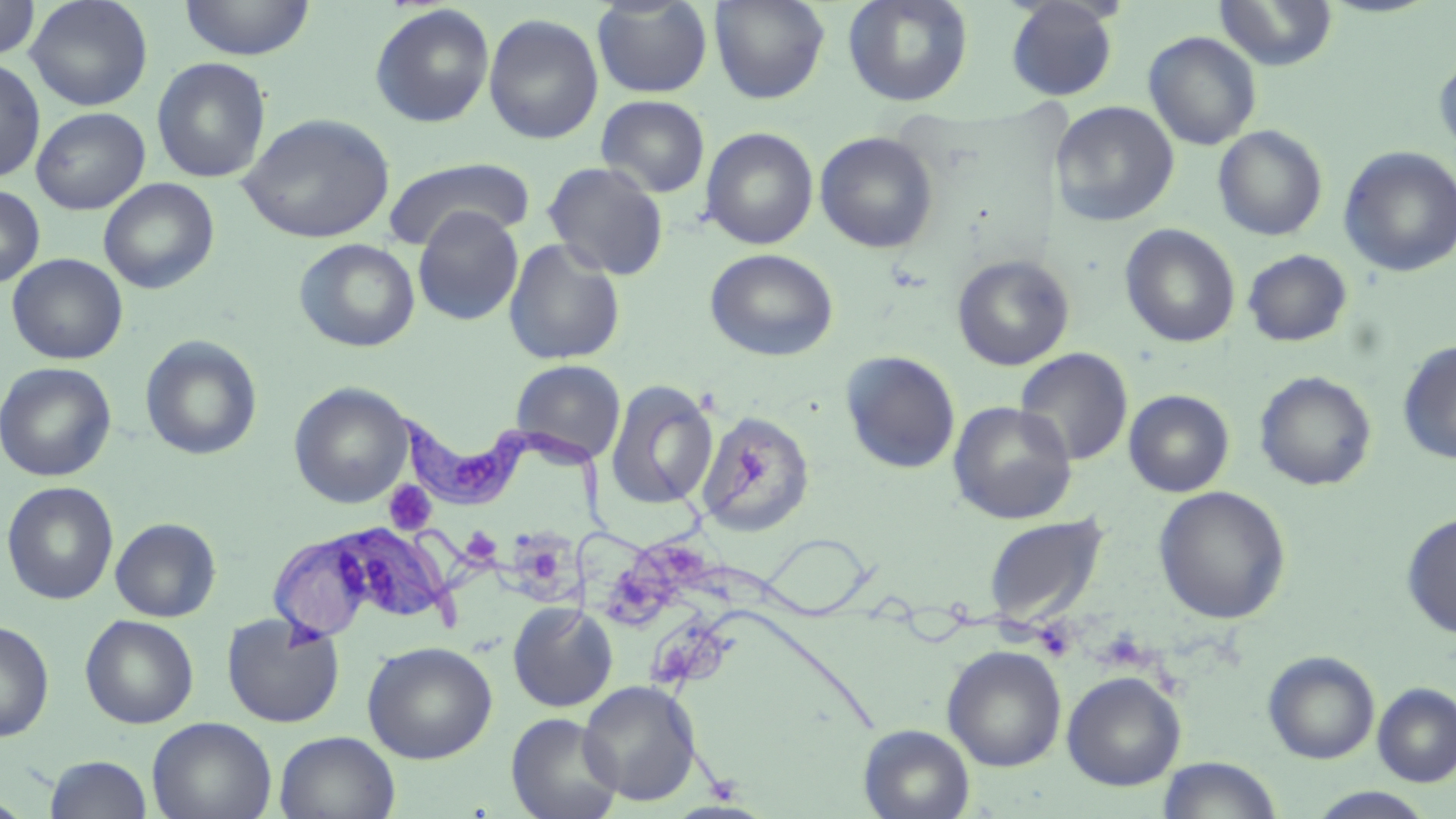
Summary:
  - Coordinate format: approximate bounding boxes as (x1,y1)-(x2,y2) corner pairs in pixels
  - Platelet locations: (383,481)-(436,535), (1032,618)-(1077,661), (1095,628)-(1152,671)
  - Uninfected red blood cell locations: (0,0)-(40,61), (25,0)-(153,111), (178,0)-(315,60), (591,0)-(713,98), (709,0)-(830,104), (842,0)-(973,107), (1005,0)-(1120,101), (1214,0)-(1338,71), (369,3)-(495,129), (483,13)-(604,145), (1143,31)-(1262,151), (1433,55)-(1456,159), (152,57)-(271,183), (0,58)-(45,183), (596,94)-(710,197), (1050,101)-(1179,228), (31,107)-(149,214), (238,112)-(395,244), (1212,125)-(1328,241), (700,127)-(819,249), (815,132)-(938,254), (1338,146)-(1456,278), (382,157)-(534,251), (542,161)-(670,281), (99,177)-(219,294), (0,185)-(45,289), (412,206)-(524,326), (1120,224)-(1240,348), (294,238)-(421,353), (502,238)-(626,366), (705,248)-(838,361), (1242,249)-(1351,347), (6,253)-(128,364), (952,255)-(1074,370), (139,335)-(263,460), (1397,340)-(1456,465), (1014,347)-(1133,466), (840,351)-(961,474), (510,359)-(626,465), (0,361)-(117,482), (1254,371)-(1377,491), (605,380)-(719,510), (289,382)-(414,508), (1123,389)-(1234,497), (948,401)-(1077,524), (696,411)-(815,537), (1,481)-(119,605), (1154,486)-(1291,624), (1401,512)-(1456,637), (982,513)-(1110,626), (110,517)-(221,622), (507,601)-(618,712), (221,611)-(345,728), (80,614)-(199,728), (0,620)-(54,743), (362,640)-(498,764), (942,644)-(1067,772), (1263,651)-(1380,764), (1062,670)-(1186,791), (578,679)-(702,806), (1373,682)-(1456,787), (506,712)-(623,819), (147,716)-(277,819), (858,724)-(975,819), (274,731)-(400,818), (44,754)-(152,818), (1156,756)-(1283,819), (1306,787)-(1437,819), (0,795)-(34,818)
  - Trypanosoma brucei locations: (397,412)-(624,538), (258,522)-(610,641)
  - Slide-level diagnosis: Trypanosoma brucei
  - Preparation: thin blood film
  - Image size: 1456×819 pixels
  - Field of view: single
  - Stain: May-Grünwald-Giemsa
  - Magnification: 1000x
  - Modality: optical microscopy